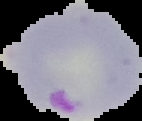 Image is 142×121 pixels. Result: Plasmodium parasites identified. Cell region segmented out of the field of view; the surrounding area is masked to black. From a thin blood smear.